Report the malaria status of this cell.
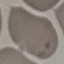
It is uninfected.

Summary:
  - Capture: smartphone through the microscope eyepiece
  - Stain: Giemsa
  - Preparation: thin blood smear
  - Image type: cell patch, automatically extracted from a larger field of view and resized to 64 × 64 pixels